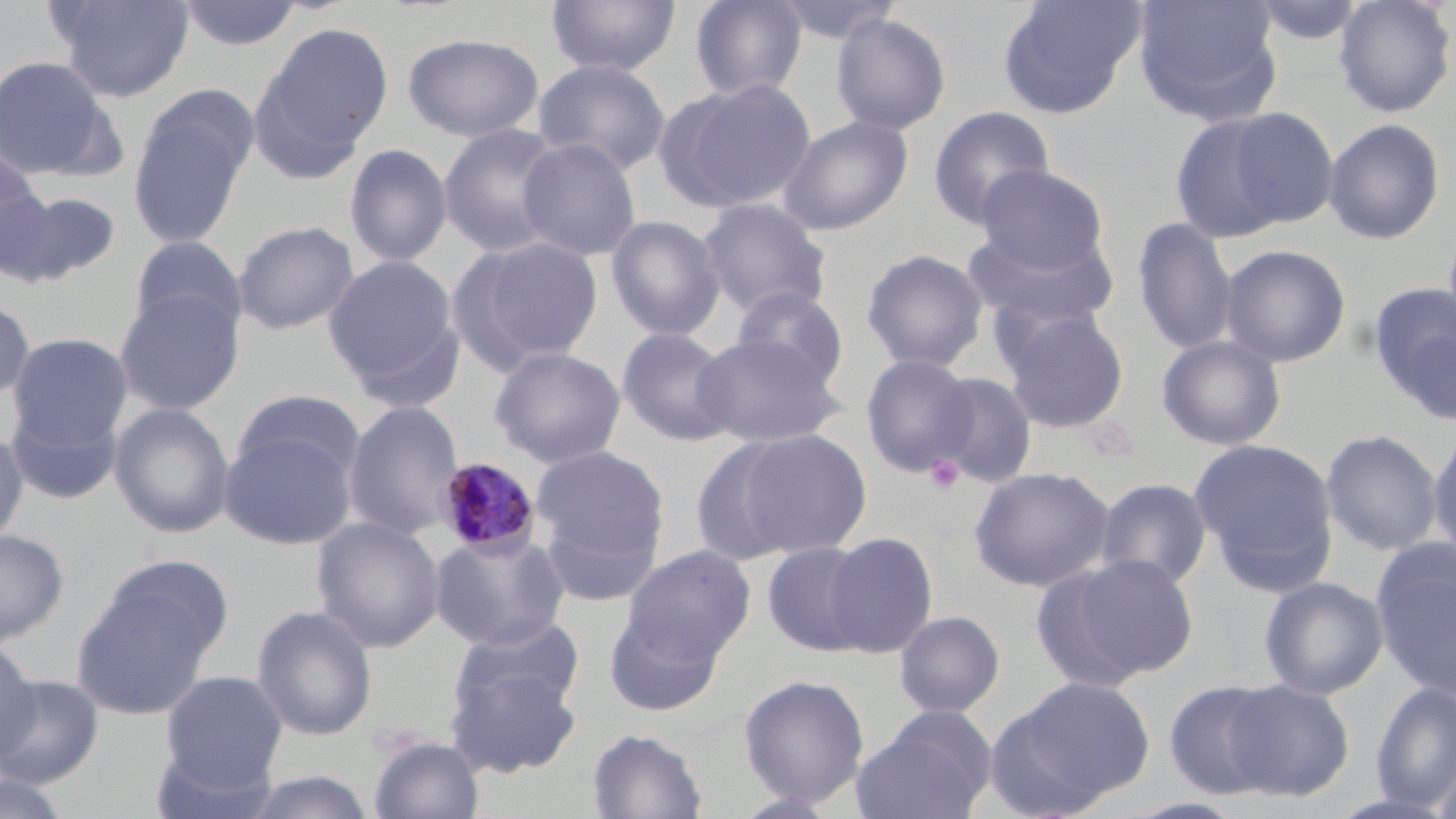
{
  "slide_level_diagnosis": "Plasmodium malariae",
  "stain": "May-Grünwald-Giemsa",
  "plasmodium_malariae_infected_red_blood_cell_locations": "approximate bounding boxes as (x1,y1)-(x2,y2) corner pairs in pixels: (436,457)-(542,558)",
  "field_of_view": "single",
  "modality": "optical microscopy",
  "magnification": "1000x",
  "image_size": "1456×819 pixels",
  "preparation": "thin blood film",
  "uninfected_red_blood_cell_locations": "approximate bounding boxes as (x1,y1)-(x2,y2) corner pairs in pixels: (49,0)-(194,102), (178,0)-(303,52), (546,0)-(681,77), (689,0)-(808,102), (768,0)-(903,47), (998,0)-(1146,118), (1132,0)-(1282,123), (1246,0)-(1369,47), (1333,0)-(1455,117), (830,13)-(952,136), (260,22)-(394,156), (401,33)-(544,143), (0,55)-(115,179), (532,58)-(671,175), (247,69)-(370,185), (656,77)-(817,215), (128,104)-(251,248), (927,106)-(1056,230), (1221,107)-(1339,230), (1169,111)-(1306,243), (778,115)-(913,236), (1323,118)-(1446,245), (438,123)-(567,257), (516,137)-(642,261), (344,143)-(453,267), (0,155)-(52,278), (973,165)-(1110,274), (2,186)-(121,289), (697,198)-(833,318), (605,215)-(727,341), (1132,216)-(1238,355), (233,220)-(359,335), (963,225)-(1119,333), (129,235)-(247,340), (454,235)-(605,371), (1220,244)-(1351,367), (861,248)-(989,373), (323,254)-(463,399), (1368,283)-(1456,420), (730,285)-(850,393), (114,289)-(244,415), (1,295)-(35,407), (1000,306)-(1131,434), (615,327)-(738,446), (691,332)-(843,449), (6,333)-(133,450), (1157,335)-(1286,451), (488,346)-(626,469), (860,353)-(978,477), (928,371)-(1039,488), (232,389)-(366,487), (4,400)-(123,505), (343,400)-(464,540), (109,403)-(235,539), (219,426)-(358,550), (0,428)-(29,550), (719,428)-(874,560), (1320,429)-(1444,556), (1427,429)-(1456,567), (1189,438)-(1340,593), (530,443)-(671,593), (968,466)-(1115,592), (1094,477)-(1213,589), (311,516)-(445,653), (0,528)-(68,644), (429,530)-(571,651), (822,532)-(938,657), (762,541)-(876,656), (1372,542)-(1456,701), (620,545)-(756,667), (96,554)-(235,667), (1039,554)-(1201,688), (1259,577)-(1388,699), (72,581)-(217,719), (252,604)-(378,741), (603,607)-(727,716), (894,610)-(1006,718), (450,616)-(585,724), (0,641)-(39,762), (445,659)-(583,778), (159,670)-(288,791), (737,673)-(870,809), (0,674)-(103,788), (1002,675)-(1155,810), (1164,680)-(1286,799), (1223,680)-(1354,801), (1370,680)-(1456,813), (850,708)-(998,819), (587,727)-(708,818), (366,734)-(485,819), (1431,746)-(1456,819), (238,769)-(377,818), (0,772)-(75,819), (1122,797)-(1252,819)",
  "platelet_locations": "approximate bounding boxes as (x1,y1)-(x2,y2) corner pairs in pixels: (923,455)-(964,494)"
}